Describe the morphology of the erythrocytes.
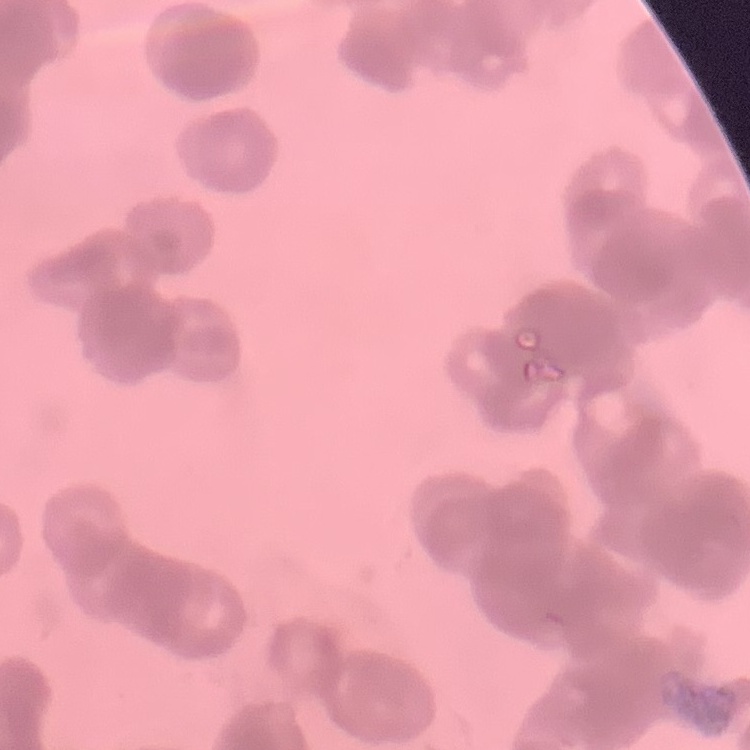

They show rouleaux formation.

Field's or Giemsa stain. Square crop of a larger photomicrograph. Thin peripheral smear.